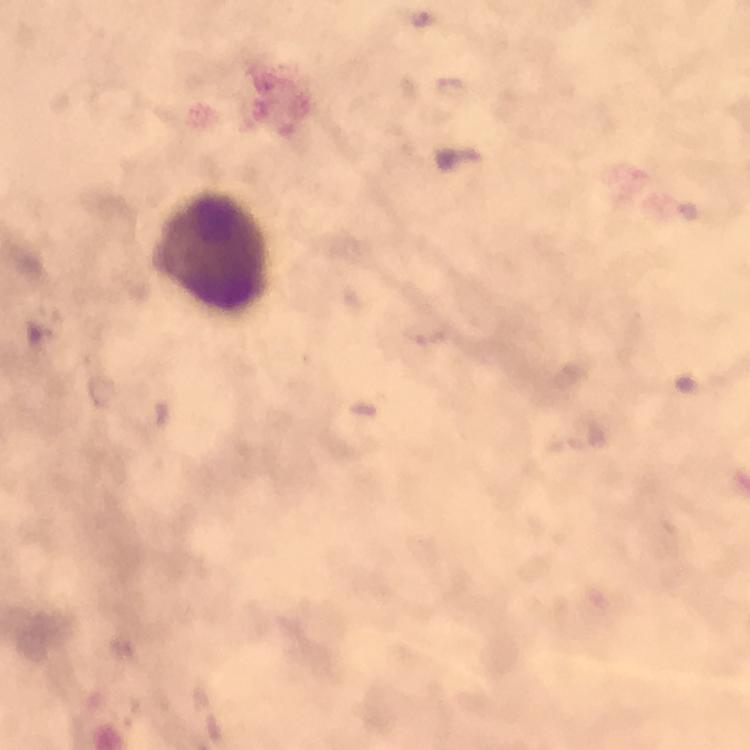

context = from a malaria diagnostic workup
capture = smartphone mounted on the microscope
Plasmodium parasites = none detected
image size = 750×750 pixels
preparation = thick blood smear
stain = Giemsa
magnification = 100x
leukocyte locations = approximate centers as (x, y) in pixels: (211, 254)
cropped from = a single field of view
immersion oil = used